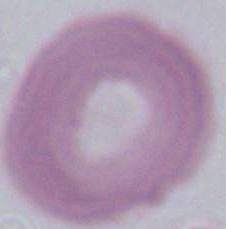
{
  "magnification": "1000x",
  "identification": "erythrocyte",
  "modality": "micrograph"
}